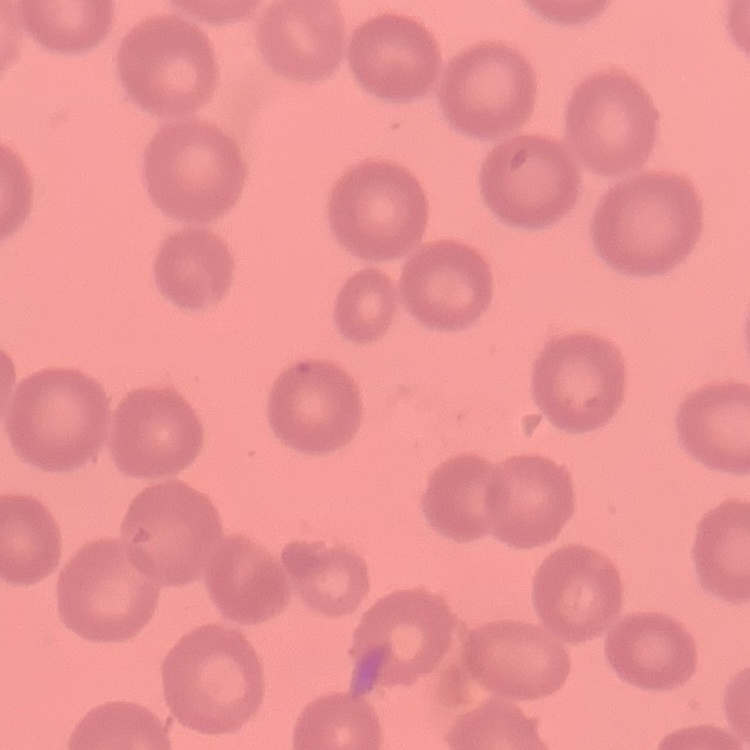

erythrocyte morphology = no rouleaux formation
stain = Field's or Giemsa
image type = one tile cut from a larger photomicrograph
preparation = thin blood smear